Locate every Plasmodium parasite and every leukocyte.
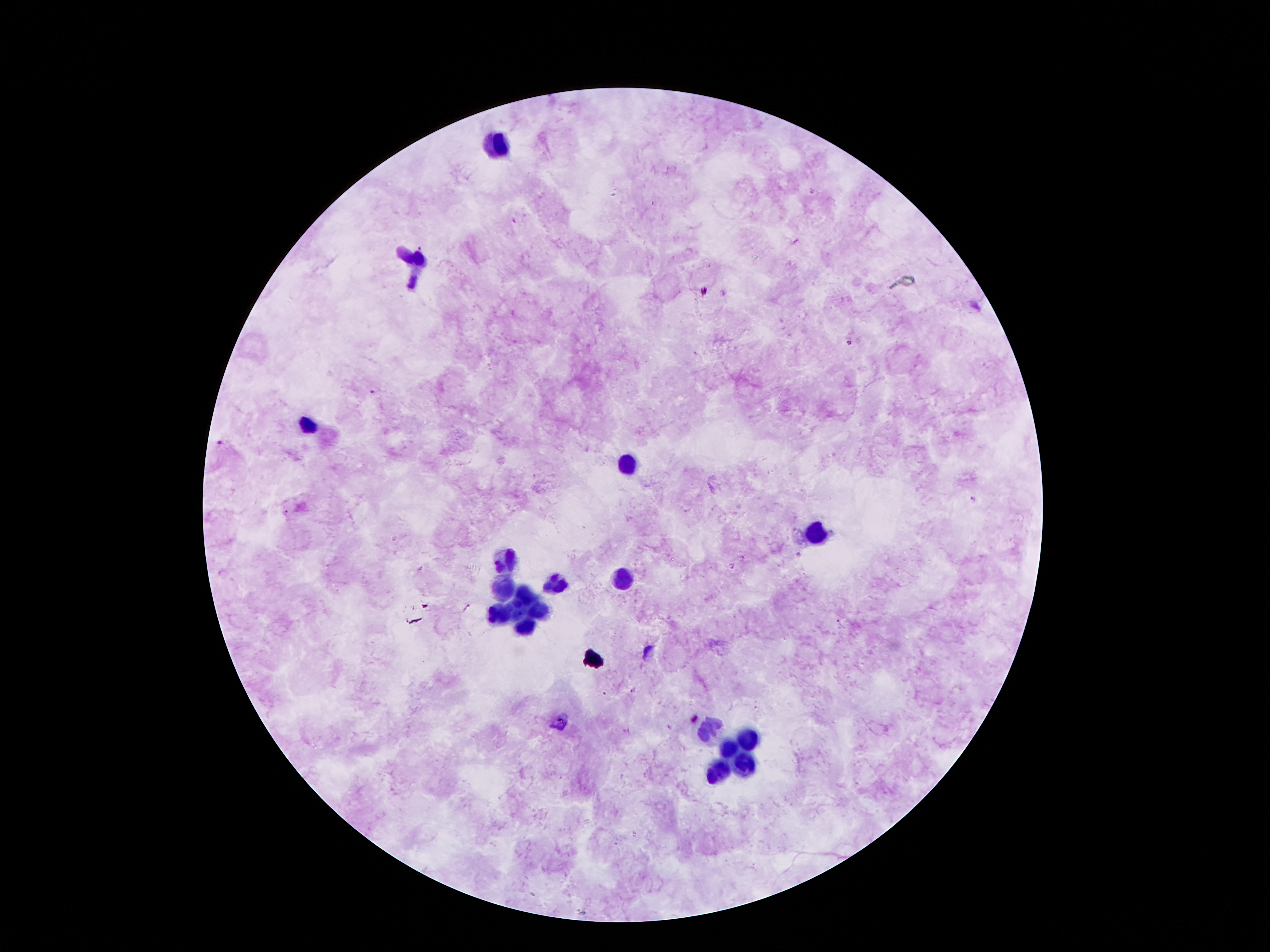

Approximate object centers, in pixels from the top-left corner.
Plasmodium parasites: (x=422, y=247), (x=849, y=343), (x=372, y=391), (x=217, y=443), (x=971, y=498), (x=287, y=513), (x=797, y=555), (x=732, y=565), (x=422, y=570), (x=467, y=607), (x=838, y=622), (x=633, y=690).
Leukocytes: (x=500, y=141), (x=416, y=264), (x=309, y=423), (x=629, y=461), (x=817, y=536), (x=506, y=559), (x=622, y=579), (x=554, y=580), (x=503, y=588), (x=524, y=596), (x=515, y=612), (x=496, y=614), (x=537, y=614), (x=525, y=628), (x=709, y=730), (x=747, y=737), (x=730, y=748), (x=741, y=764), (x=718, y=775).

magnification = 100x
image size = 1270×952 pixels
capture = smartphone camera through the microscope eyepiece
preparation = thick blood smear
patient malaria status = positive for Plasmodium falciparum
field of view = one from this slide
stain = Giemsa